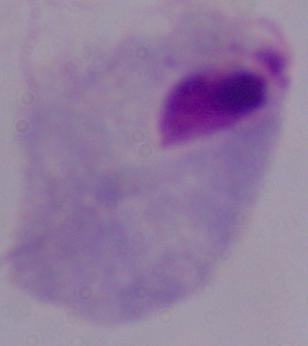

Captured at 1000x magnification. A trichomonad is shown. Photomicrograph.